Assess the morphology of the red blood cells.
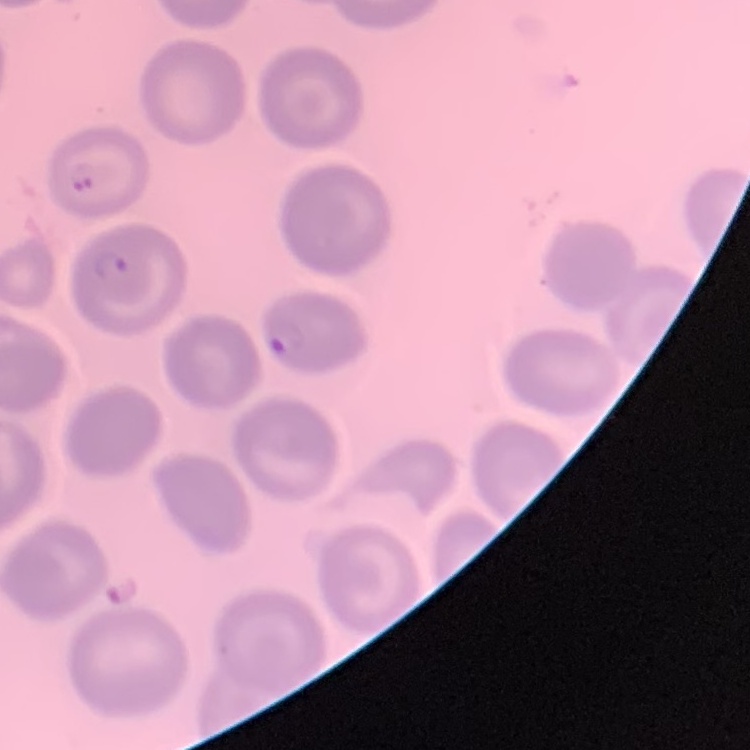

No rouleaux formation.

{
  "stain": "Field's or Giemsa",
  "preparation": "thin blood film",
  "image_type": "square crop of a larger photomicrograph"
}